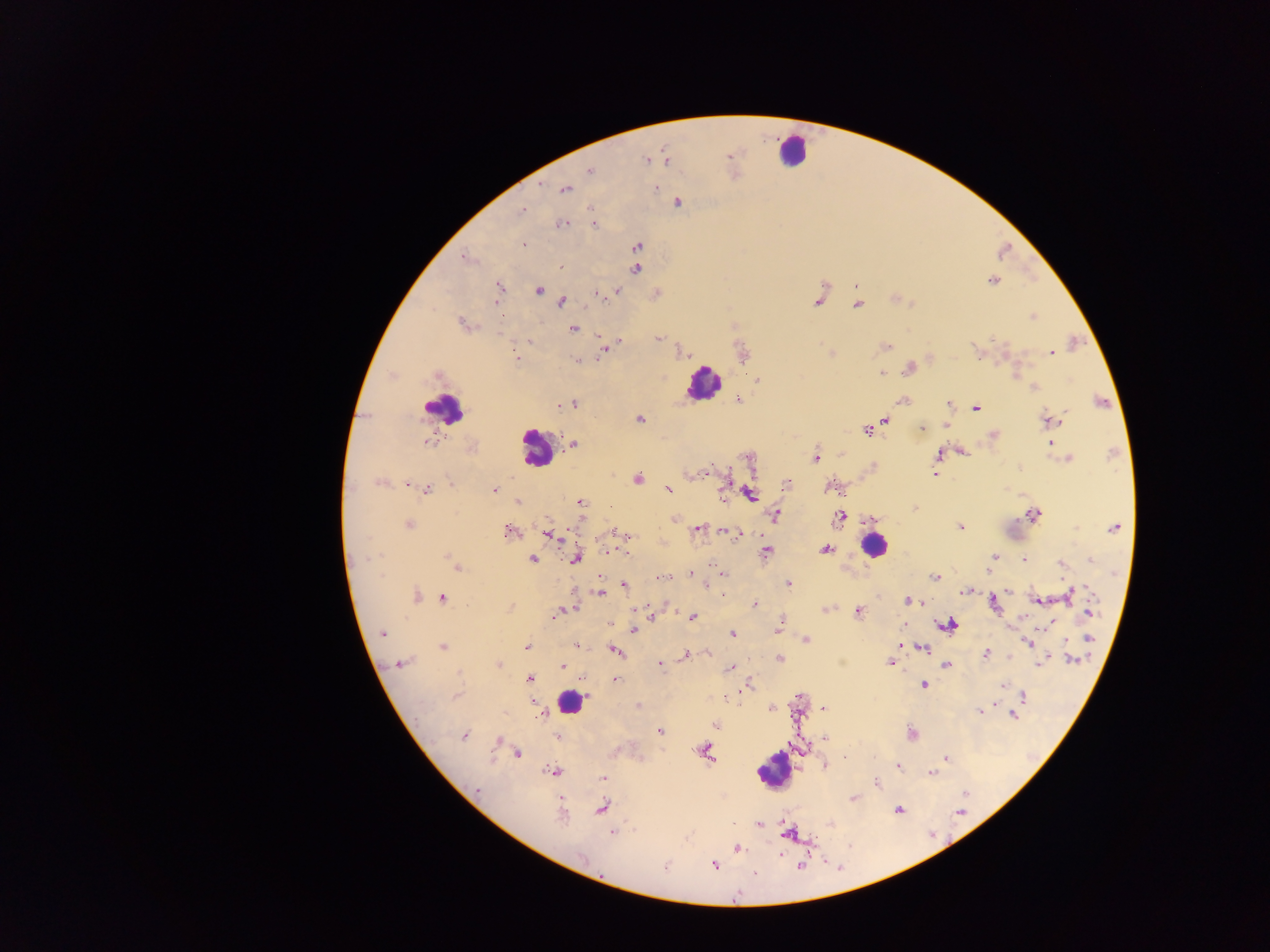

Approximate centers as [x, y] in pixels.
Summary:
  - Plasmodium parasite locations: [729, 155], [647, 159], [665, 160], [589, 171], [654, 187], [564, 189], [677, 203], [593, 210], [521, 211], [561, 223], [593, 224], [522, 244], [636, 246], [465, 256], [560, 265], [635, 268], [992, 280], [855, 286], [499, 288], [538, 290], [616, 291], [598, 294], [656, 294], [818, 299], [895, 299], [560, 301], [857, 305], [1033, 316], [463, 324], [573, 328], [599, 337], [659, 338], [528, 341], [617, 341], [884, 346], [606, 348], [681, 351], [742, 352], [977, 352], [829, 353], [1052, 353], [930, 358], [518, 359], [576, 360], [909, 367], [881, 373], [438, 375], [757, 380], [1034, 387], [738, 399], [903, 400], [1101, 401], [560, 404], [573, 404], [947, 404], [975, 408], [639, 418], [884, 419], [1048, 420], [946, 424], [922, 428], [867, 430], [994, 435], [429, 440], [1051, 442], [572, 444], [471, 448], [961, 450], [840, 454], [938, 454], [815, 457], [748, 458], [1067, 458], [702, 473], [934, 473], [637, 478], [727, 478], [379, 481], [786, 483], [409, 484], [832, 486], [418, 487], [493, 488], [426, 489], [669, 489], [749, 494], [518, 502], [579, 503], [914, 508], [775, 514], [1033, 515], [839, 517], [673, 518], [869, 519], [409, 524], [961, 527], [1114, 528], [698, 529], [510, 531], [725, 531], [549, 534], [740, 534], [624, 535], [825, 549], [608, 550], [766, 551], [994, 556], [576, 557], [1024, 558], [532, 559], [1091, 559], [1060, 565], [456, 566], [720, 573], [690, 574], [936, 576], [662, 578], [787, 583], [624, 584], [967, 591], [599, 593], [722, 594], [415, 595], [1069, 595], [441, 597], [907, 600], [1036, 600], [993, 601], [924, 602], [755, 604], [825, 608], [564, 609], [858, 611], [557, 612], [1088, 612], [649, 615], [691, 618], [1051, 622], [607, 623], [948, 624], [901, 625], [1011, 625], [778, 626], [634, 630], [381, 633], [733, 633], [1088, 637], [805, 639], [1029, 643], [576, 644], [527, 646], [901, 646], [442, 647], [922, 647], [615, 650], [708, 653], [987, 653], [685, 655], [1009, 656], [779, 659], [1070, 659], [893, 660], [891, 662], [1039, 662], [660, 663], [399, 664], [946, 664], [497, 665], [562, 665], [731, 668], [529, 678], [616, 679], [746, 684], [924, 684], [1002, 685], [456, 695], [1022, 697], [638, 705], [772, 708], [821, 709], [540, 710], [978, 710], [543, 712], [1013, 715], [715, 725], [660, 730], [912, 733], [463, 736], [558, 737], [824, 738], [498, 740], [705, 751], [518, 753], [946, 759], [825, 765], [898, 767], [553, 772], [930, 772], [603, 778], [875, 783], [477, 789], [853, 798], [601, 808], [898, 809], [561, 811], [758, 824], [612, 831], [736, 848], [714, 864], [665, 866]
  - Leukocyte locations: [792, 151], [704, 383], [442, 409], [536, 447], [874, 545], [569, 702], [774, 770]
  - Preparation: thick blood film
  - Image size: 1270×952 pixels
  - Country: Ghana
  - Capture: mobile-phone photograph through a microscope
  - Field of view: single